State which parasite is depicted.
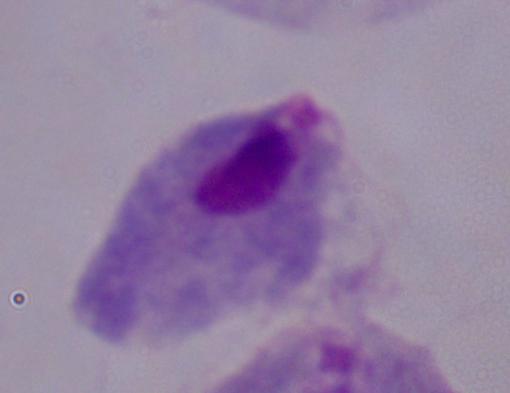
This is a trichomonad.

Summary:
  - Modality: micrograph
  - Magnification: 1000x